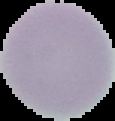 Result: no malaria parasites seen. Cell region segmented out of the field of view; the surrounding area is masked to black. Image is 115×121 pixels. From a thin blood smear.